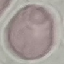

Summary:
  - Malaria status: uninfected
  - Stain: Giemsa
  - Preparation: thin smear
  - Image type: cell patch, automatically extracted from a larger field of view and resized to 64 × 64 pixels
  - Capture: smartphone camera at the microscope eyepiece